State which parasite is depicted.
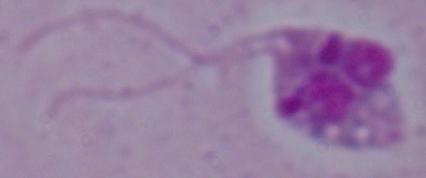
This is Leishmania.

Summary:
  - Modality: micrograph
  - Magnification: 1000x